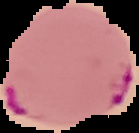
Result: Plasmodium parasites detected. Image is 139×133 pixels. Cell region segmented out of the field of view; the surrounding area is masked to black. From a thin blood smear.